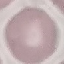 Malaria status: uninfected. Automatically extracted cell patch, resized to 64 × 64 pixels. Thin smear of blood. Photographed with a smartphone camera at the microscope eyepiece. Giemsa-stained preparation.